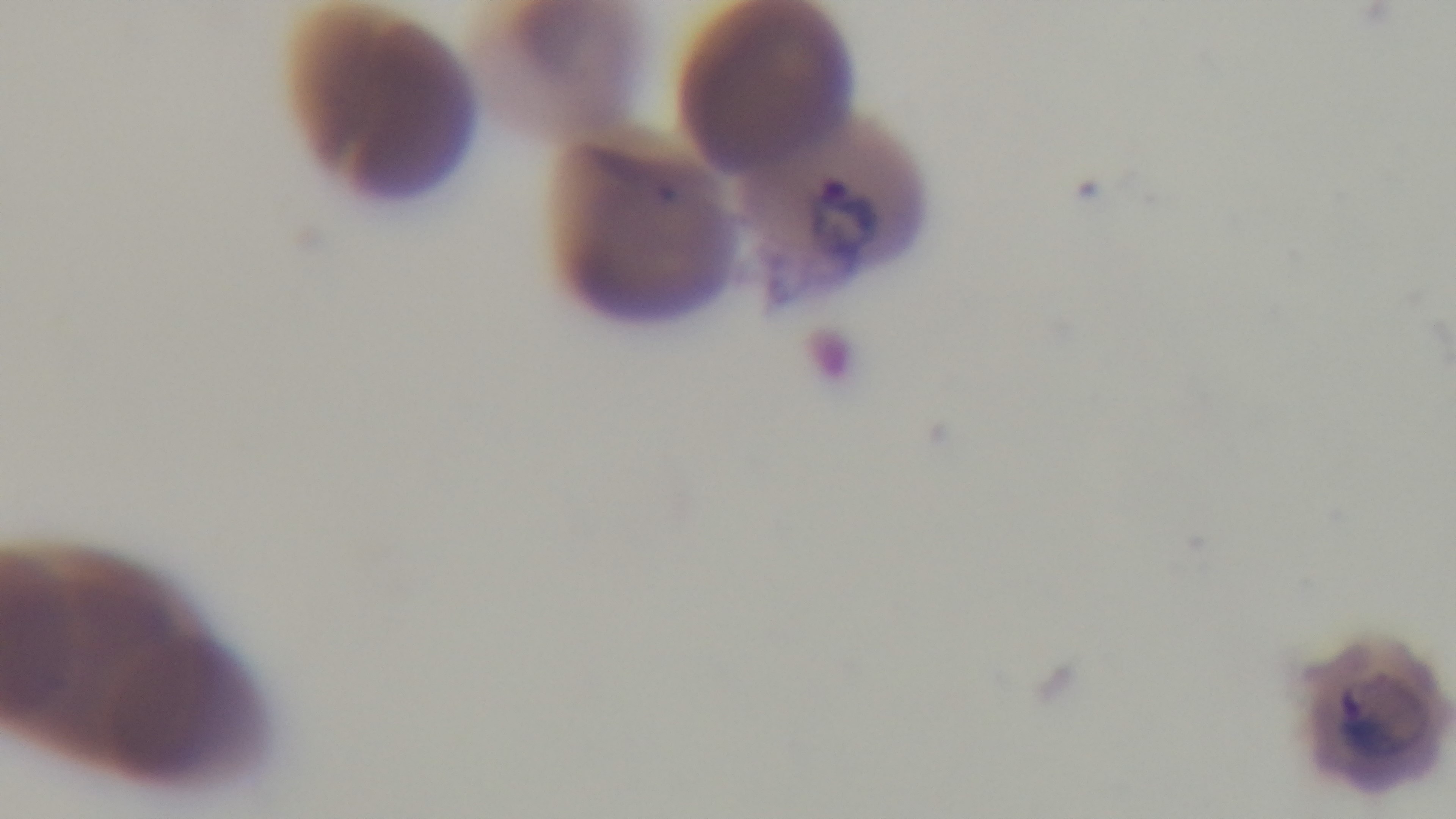

Summary:
  - Capture: mounted 4K digital camera
  - Stain: Giemsa
  - Malaria status: infected
  - Preparation: thin smear
  - Objective: 100x oil immersion
  - Field of view: one from the slide
  - Modality: light microscopy